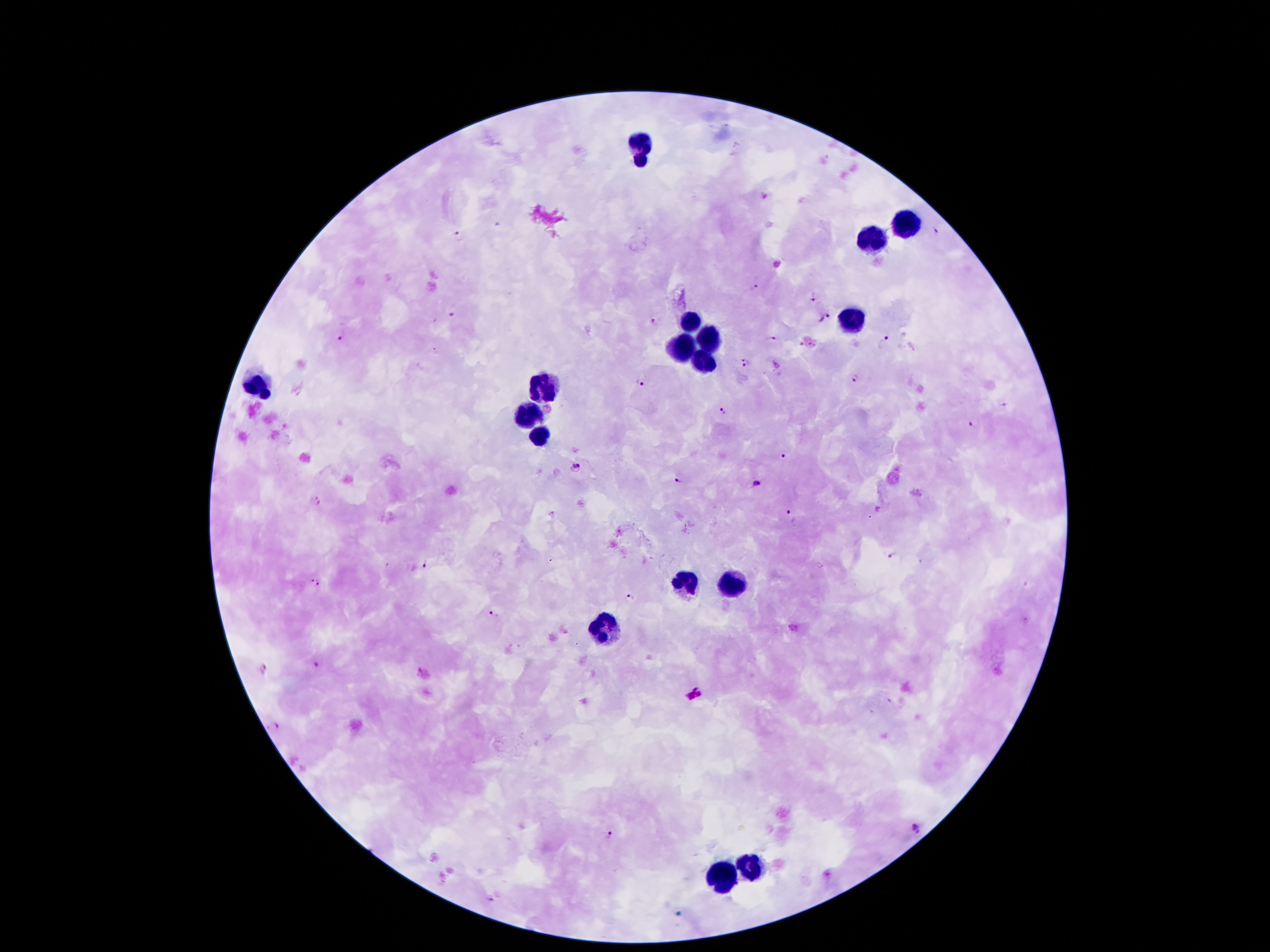

{
  "capture": "smartphone camera through the microscope eyepiece",
  "image_size": "1270×952 pixels",
  "plasmodium_parasite_locations": "approximate object centers, in pixels from the top-left corner: (x=936, y=231), (x=457, y=235), (x=755, y=287), (x=813, y=298), (x=452, y=310), (x=824, y=319), (x=654, y=321), (x=343, y=338), (x=772, y=340), (x=885, y=340), (x=745, y=363), (x=856, y=376), (x=642, y=383), (x=1005, y=405), (x=724, y=410), (x=973, y=424), (x=783, y=457), (x=576, y=465), (x=679, y=479), (x=757, y=481), (x=315, y=499), (x=790, y=512), (x=892, y=556), (x=424, y=563), (x=314, y=581), (x=628, y=596), (x=493, y=614), (x=317, y=662), (x=263, y=667), (x=422, y=670), (x=694, y=695), (x=275, y=724), (x=918, y=830), (x=610, y=835), (x=491, y=899)",
  "magnification": "100x",
  "leukocyte_locations": "approximate object centers, in pixels from the top-left corner: (x=639, y=136), (x=639, y=162), (x=907, y=223), (x=874, y=238), (x=691, y=315), (x=851, y=315), (x=710, y=341), (x=682, y=350), (x=702, y=369), (x=256, y=382), (x=540, y=391), (x=529, y=416), (x=542, y=436), (x=685, y=580), (x=732, y=584), (x=605, y=628), (x=751, y=864), (x=723, y=877)",
  "patient_malaria_status": "positive for Plasmodium falciparum",
  "preparation": "thick blood film",
  "stain": "Giemsa",
  "field_of_view": "one from this slide"
}